Classify the preparation.
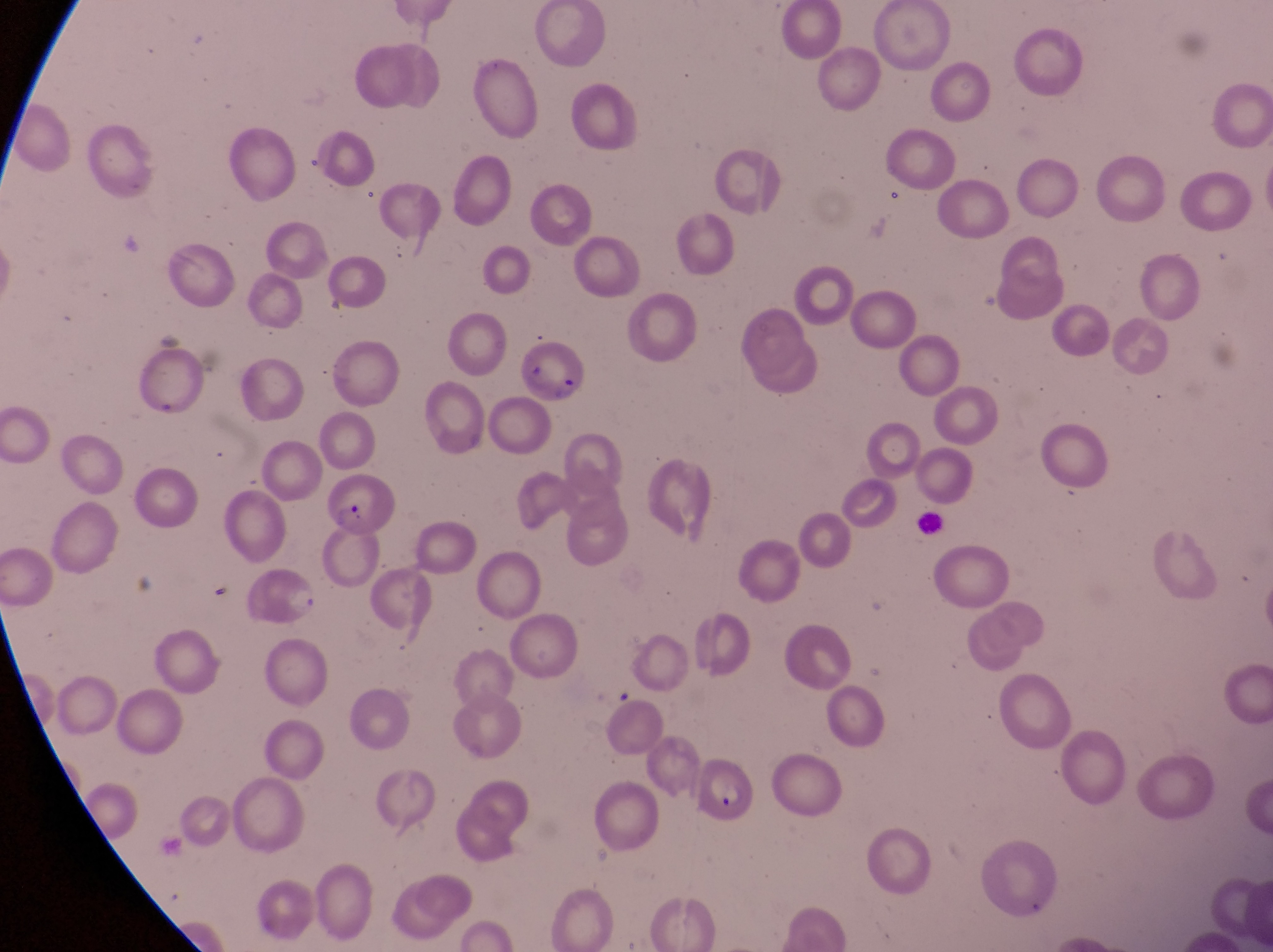
This is a thin smear.

field_of_view: single
parasitised_red_blood_cell_locations: 'approximate bounding boxes as (left, top, right, bottom) in pixels: (512, 344, 592, 407), (314, 477, 402, 540), (699, 761, 761, 833)'
image_size: 1273×952 pixels
country: Uganda
capture: smartphone photograph through the eyepiece of an Olympus CX-23 microscope
magnification: 1000x